Assess this cell for malaria.
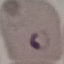

It is parasitized.

image_type: cell patch, automatically extracted from a larger field of view and resized to 64 × 64 pixels
capture: smartphone through the microscope eyepiece
stain: Giemsa
preparation: thin blood film